Locate every blood parasite and identify its species.
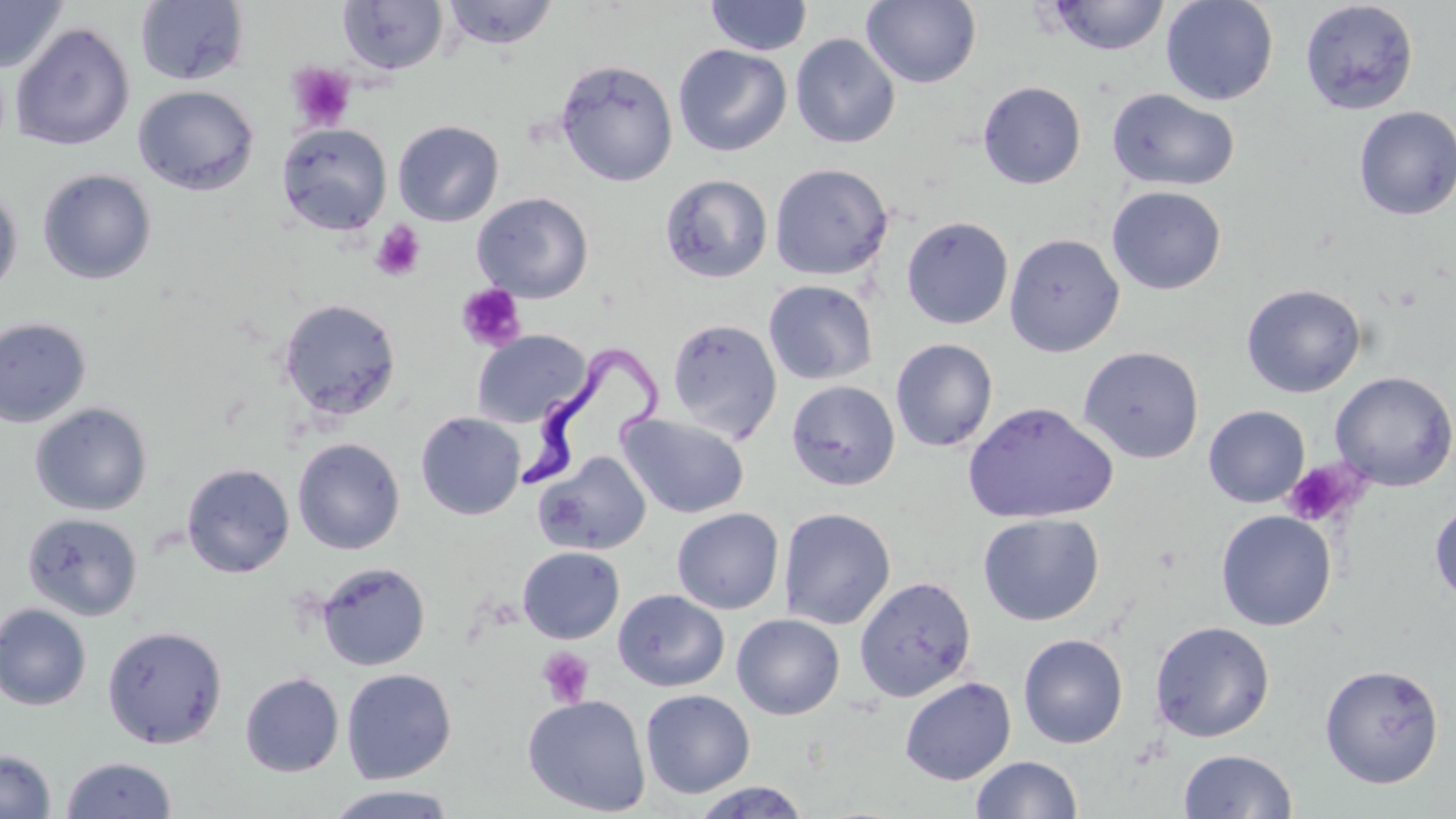
Approximate bounding boxes as (x1,y1)-(x2,y2) corner pairs in pixels.
Trypanosoma brucei: (523,340)-(661,493).
No Plasmodium falciparum, Plasmodium ovale, Plasmodium malariae, Plasmodium vivax, or Babesia divergens observed.

slide-level diagnosis = Trypanosoma brucei
stain = May-Grünwald-Giemsa
magnification = 1000x
preparation = thin blood film
uninfected red blood cell locations = approximate bounding boxes as (x1,y1)-(x2,y2) corner pairs in pixels: (0,0)-(69,74), (705,0)-(813,56), (1047,0)-(1170,56), (1160,0)-(1278,106), (134,1)-(250,86), (338,1)-(448,75), (441,1)-(559,50), (861,1)-(982,88), (1299,1)-(1419,115), (9,22)-(135,151), (790,33)-(901,149), (673,44)-(792,157), (555,59)-(678,187), (978,81)-(1087,189), (132,85)-(259,196), (1106,88)-(1240,192), (1353,106)-(1456,220), (392,120)-(504,226), (276,123)-(392,235), (769,163)-(893,280), (37,168)-(157,285), (660,174)-(773,283), (0,184)-(23,302), (1107,186)-(1227,295), (472,192)-(593,303), (901,215)-(1014,329), (1004,233)-(1125,357), (763,280)-(878,385), (1240,283)-(1367,398), (277,298)-(402,423), (0,317)-(92,429), (667,318)-(783,443), (472,329)-(592,428), (890,339)-(998,452), (1078,345)-(1204,464), (1330,371)-(1456,491), (786,380)-(901,491), (962,401)-(1118,524), (29,402)-(153,516), (1203,405)-(1310,507), (416,412)-(526,520), (618,414)-(750,518), (292,438)-(405,555), (534,453)-(652,554), (181,463)-(295,578), (1429,500)-(1456,606), (778,507)-(896,630), (671,508)-(784,614), (1215,510)-(1337,631), (22,512)-(144,621), (977,513)-(1104,626), (517,546)-(625,644), (316,561)-(431,671), (854,576)-(977,701), (612,588)-(729,692), (0,603)-(92,711), (731,613)-(845,720), (1150,621)-(1275,743), (102,625)-(228,749), (1018,633)-(1128,748), (1319,663)-(1444,789), (340,668)-(457,783), (240,672)-(344,777), (900,676)-(1016,785), (640,689)-(756,798), (522,694)-(651,816), (0,749)-(57,819), (1178,749)-(1298,818), (60,755)-(177,818), (970,755)-(1083,818), (688,781)-(812,818), (322,785)-(461,819)
image size = 1456×819 pixels
field of view = one of a larger specimen
modality = optical microscopy
platelet locations = approximate bounding boxes as (x1,y1)-(x2,y2) corner pairs in pixels: (286,62)-(356,132), (369,220)-(427,282), (455,284)-(527,352), (1282,460)-(1363,528), (537,647)-(594,708)